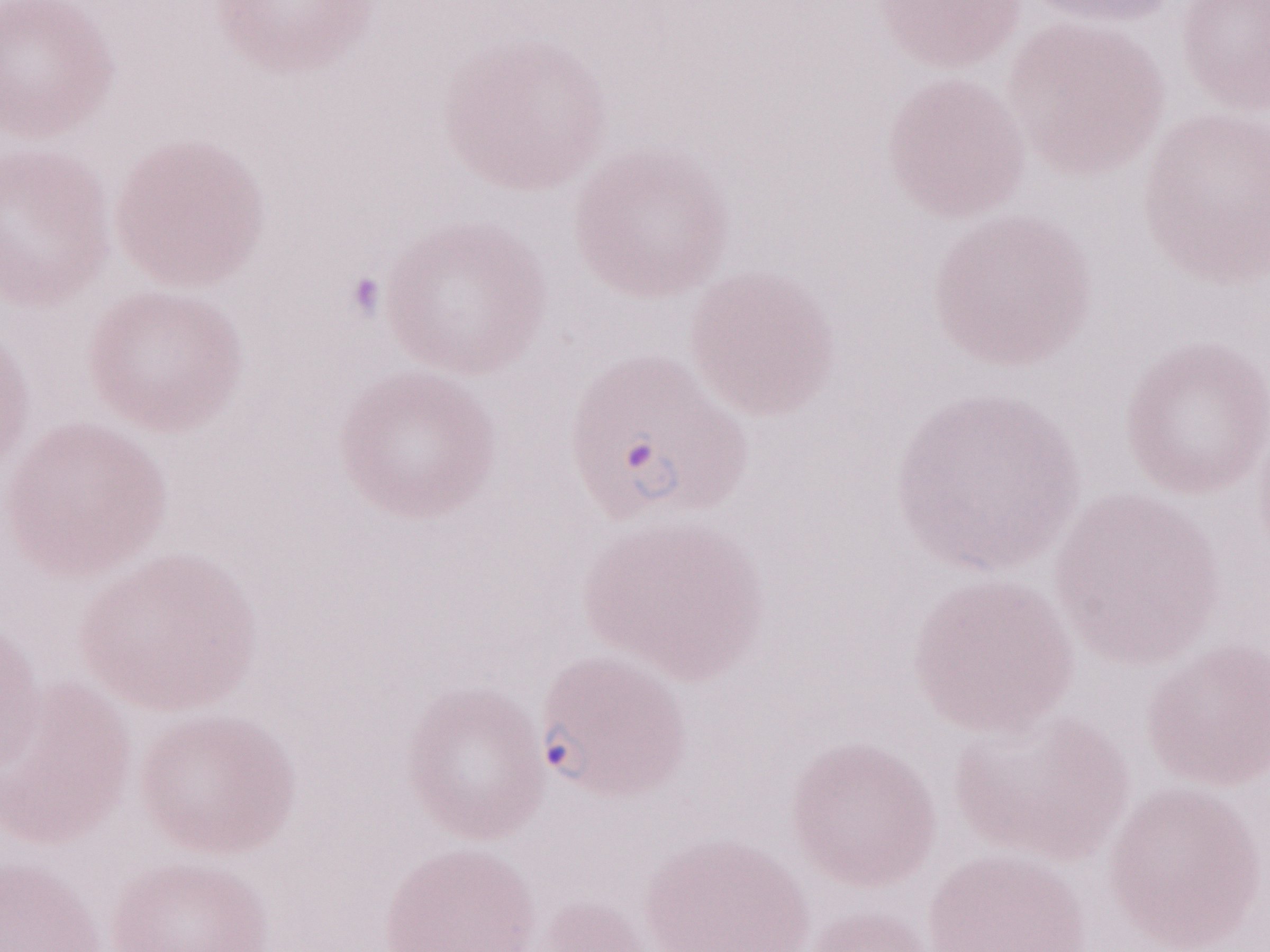 May-Grünwald-Giemsa (MGG) stain. Magnification: 1,000x. Thin blood film. One field of this slide. Olympus BX43 microscope and DP73 digital camera. Image is 1270×952 pixels. Patient-level malaria diagnosis: positive.